Report the malaria status of this cell.
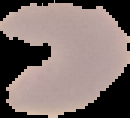
Parasitized.

The area outside the segmented cell region is set to black. From a thin blood smear. Image is 130×118 pixels.